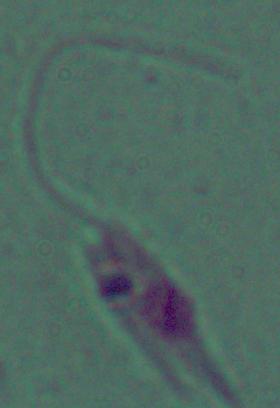

Summary:
  - Identification: Leishmania
  - Magnification: 1000x
  - Modality: micrograph